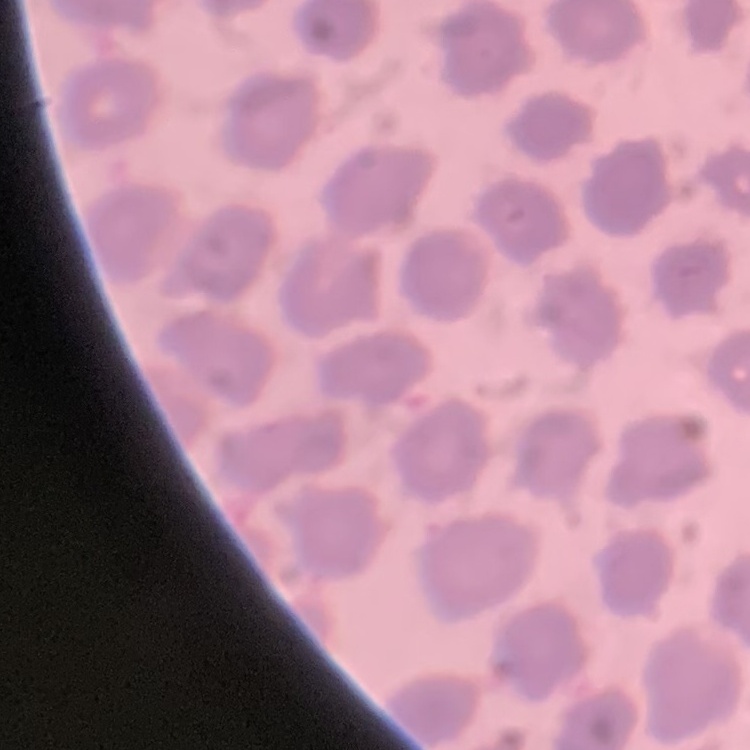 The red blood cells show no rouleaux formation. One tile cut from a larger photomicrograph. Thin peripheral smear. Stained with either Field's or Giemsa.